Outline each blood parasite and name the species.
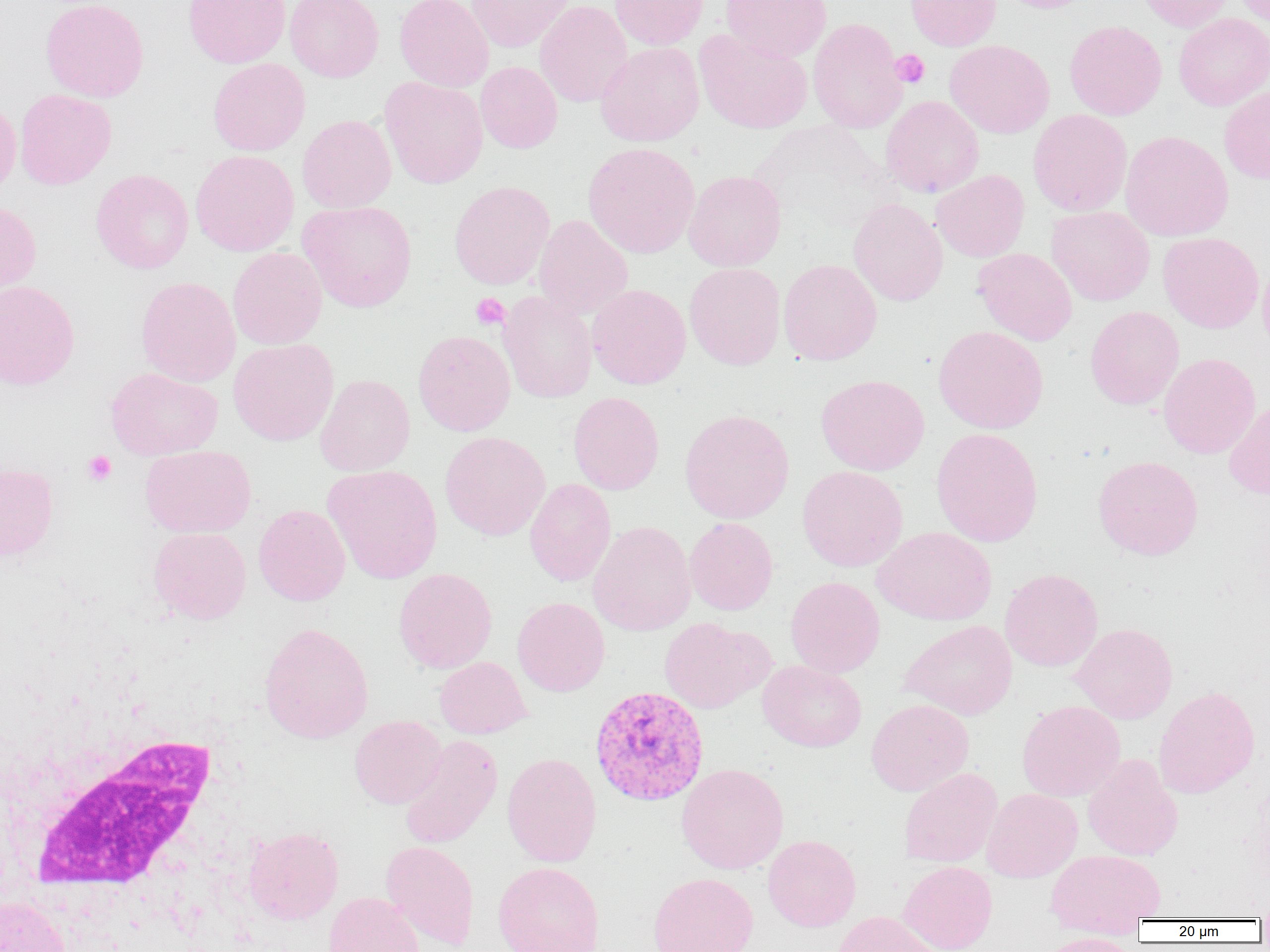
Approximate bounding boxes as [x1, y1, x2, y2] in pixels.
Plasmodium vivax-infected red blood cells: [589, 685, 709, 807].
No Plasmodium falciparum, Plasmodium ovale, Plasmodium malariae, Babesia divergens, or Trypanosoma brucei observed.

Summary:
  - Uninfected red blood cell locations: [40, 0, 149, 102], [183, 0, 290, 68], [285, 0, 383, 82], [394, 0, 493, 91], [466, 0, 573, 52], [610, 0, 708, 50], [721, 0, 831, 62], [905, 0, 1001, 51], [993, 0, 1097, 13], [1135, 0, 1234, 32], [1233, 0, 1270, 29], [534, 1, 632, 107], [1174, 13, 1270, 110], [808, 18, 907, 133], [1064, 21, 1167, 120], [693, 29, 813, 133], [944, 40, 1054, 138], [595, 42, 705, 146], [208, 58, 310, 156], [475, 61, 562, 153], [379, 76, 488, 189], [1219, 87, 1270, 184], [14, 88, 116, 190], [881, 95, 984, 197], [0, 97, 21, 199], [1028, 109, 1132, 216], [297, 114, 396, 213], [1120, 130, 1233, 241], [582, 142, 700, 258], [190, 150, 299, 256], [91, 169, 194, 274], [683, 170, 786, 271], [931, 170, 1029, 262], [449, 181, 554, 289], [848, 198, 948, 306], [0, 200, 42, 300], [297, 200, 417, 312], [1046, 206, 1155, 306], [533, 214, 633, 320], [1158, 232, 1263, 333], [227, 247, 327, 350], [973, 247, 1077, 346], [1259, 255, 1270, 359], [779, 259, 882, 365], [684, 263, 786, 370], [135, 276, 241, 387], [0, 280, 79, 390], [587, 284, 691, 389], [498, 291, 597, 403], [1085, 306, 1184, 409], [933, 325, 1049, 434], [413, 330, 515, 435], [228, 339, 339, 445], [1158, 353, 1261, 459], [105, 367, 223, 460], [315, 374, 415, 476], [816, 374, 929, 475], [568, 392, 664, 495], [1224, 397, 1270, 500], [679, 409, 794, 523], [931, 427, 1043, 547], [439, 431, 550, 541], [140, 445, 256, 538], [1092, 456, 1203, 560], [0, 463, 58, 562], [322, 464, 443, 584], [797, 466, 908, 571], [525, 478, 616, 586], [253, 504, 350, 606], [684, 517, 778, 615], [588, 521, 696, 636], [148, 527, 251, 624], [873, 527, 996, 625], [393, 567, 497, 673], [1000, 568, 1103, 672], [785, 576, 885, 678], [513, 597, 610, 696], [659, 617, 774, 714], [899, 620, 1017, 720], [1070, 622, 1178, 723], [259, 623, 373, 744], [434, 657, 532, 739], [758, 660, 867, 752], [1153, 686, 1260, 798], [866, 699, 974, 796], [1016, 700, 1125, 802], [349, 715, 446, 808], [399, 734, 503, 850], [501, 752, 602, 867], [1082, 754, 1183, 861], [676, 763, 789, 874], [898, 767, 1002, 868], [982, 788, 1082, 882], [243, 826, 343, 925], [763, 835, 861, 931], [381, 840, 479, 950], [1045, 848, 1166, 930], [898, 861, 997, 952], [492, 862, 605, 952], [647, 872, 758, 952], [324, 892, 424, 952], [0, 896, 71, 952], [831, 911, 941, 952], [1036, 932, 1141, 951]
  - Platelet locations: [890, 49, 930, 88], [471, 293, 510, 330], [82, 450, 116, 486]
  - White blood cell locations: [22, 733, 222, 914]
  - Slide-level diagnosis: Plasmodium vivax
  - Image size: 1270×952 pixels
  - Magnification: 1000x
  - Modality: light microscopy
  - Field of view: one of a larger specimen
  - Preparation: thin blood smear